Report the malaria status of this cell.
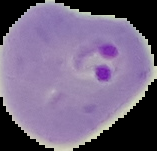
Parasitized.

Segmented cell region on a black background. Image is 157×151 pixels. From a thin blood smear.